Report the malaria status of this cell.
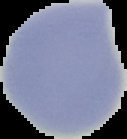
It is uninfected.

From a thin blood film. Image is 127×139 pixels. Segmented cell region on a black background.